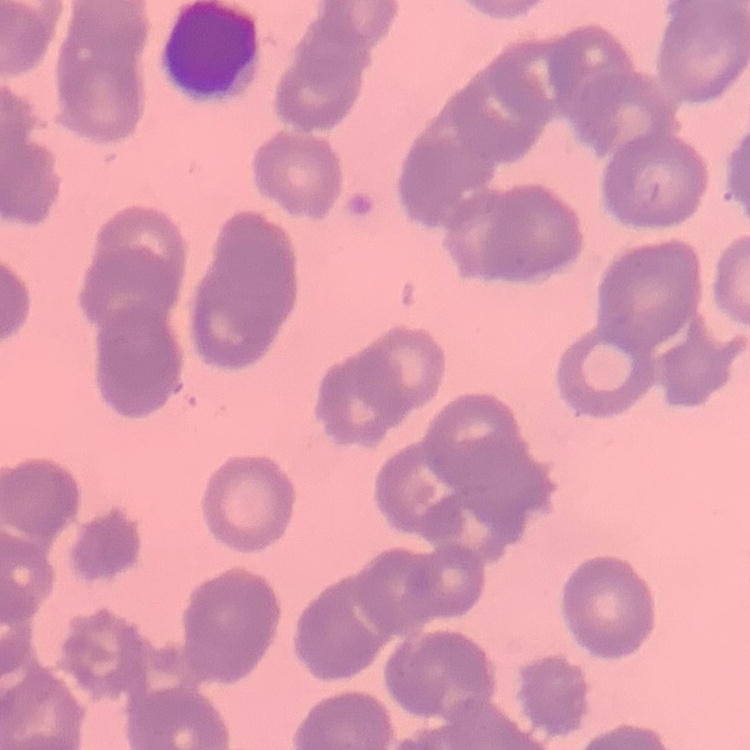
{
  "erythrocyte_morphology": "rouleaux formation",
  "preparation": "thin blood smear",
  "image_type": "one tile cut from a larger photomicrograph",
  "stain": "Field's or Giemsa"
}